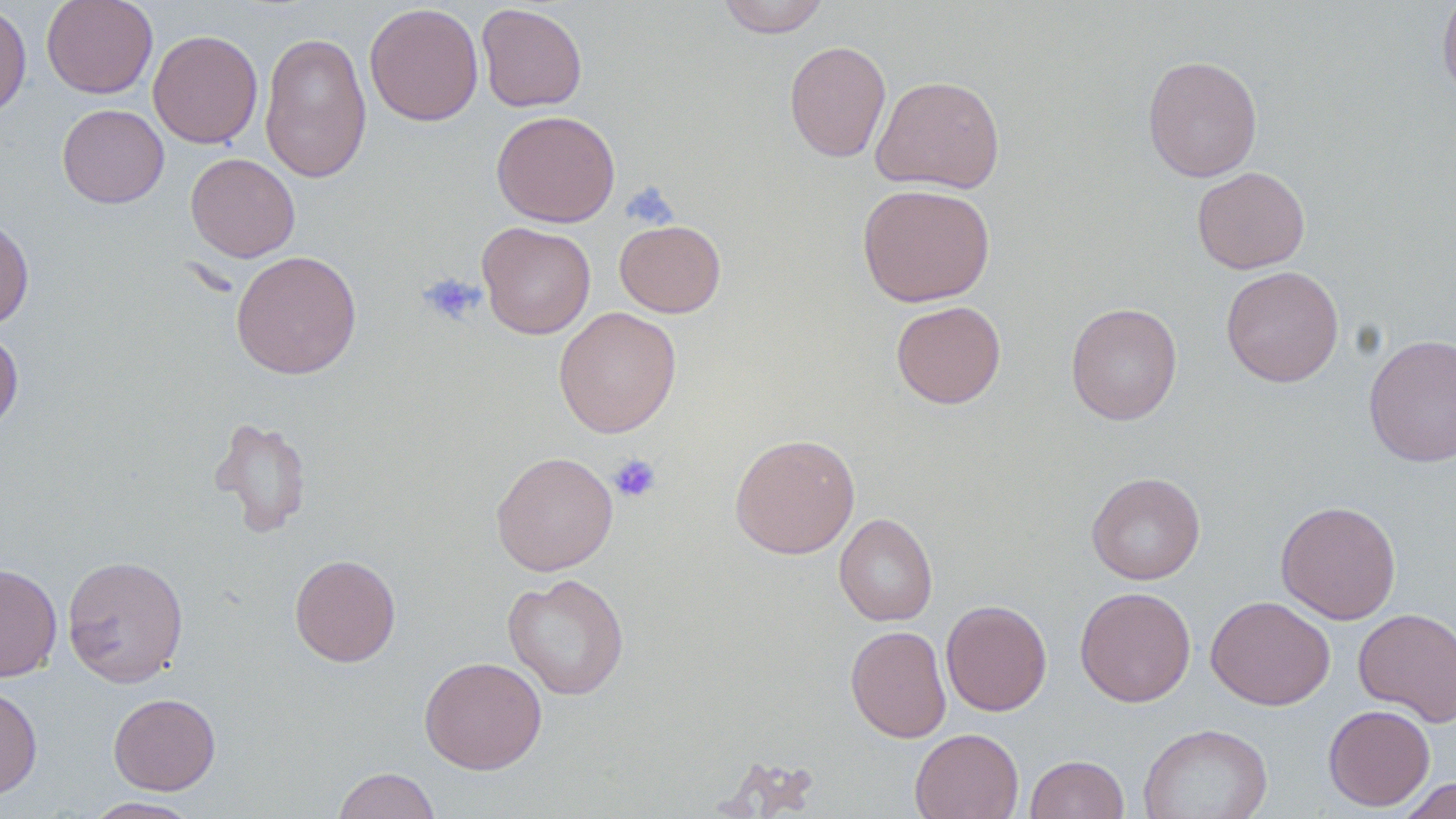
{
  "slide_level_diagnosis": "no evidence of blood parasites",
  "preparation": "thin blood smear",
  "magnification": "1000x",
  "uninfected_red_blood_cell_locations": "approximate bounding boxes as named x1/y1/x2/y2 corners in pixels: (x1=41, y1=0, x2=158, y2=99), (x1=717, y1=0, x2=830, y2=38), (x1=1437, y1=0, x2=1456, y2=106), (x1=0, y1=1, x2=32, y2=122), (x1=364, y1=3, x2=484, y2=126), (x1=476, y1=3, x2=587, y2=112), (x1=148, y1=29, x2=263, y2=149), (x1=259, y1=30, x2=372, y2=183), (x1=784, y1=40, x2=891, y2=163), (x1=1142, y1=55, x2=1263, y2=182), (x1=871, y1=75, x2=1006, y2=193), (x1=57, y1=103, x2=169, y2=208), (x1=491, y1=110, x2=620, y2=227), (x1=186, y1=152, x2=300, y2=262), (x1=1191, y1=166, x2=1310, y2=274), (x1=857, y1=182, x2=996, y2=307), (x1=0, y1=216, x2=34, y2=330), (x1=614, y1=219, x2=726, y2=318), (x1=477, y1=221, x2=596, y2=339), (x1=231, y1=250, x2=362, y2=379), (x1=1221, y1=265, x2=1344, y2=387), (x1=891, y1=300, x2=1006, y2=408), (x1=1066, y1=302, x2=1182, y2=425), (x1=554, y1=306, x2=681, y2=438), (x1=0, y1=328, x2=24, y2=435), (x1=1363, y1=333, x2=1456, y2=468), (x1=209, y1=416, x2=313, y2=538), (x1=729, y1=433, x2=860, y2=559), (x1=491, y1=451, x2=618, y2=576), (x1=1086, y1=471, x2=1205, y2=585), (x1=1275, y1=500, x2=1402, y2=624), (x1=834, y1=512, x2=938, y2=627), (x1=62, y1=554, x2=189, y2=687), (x1=289, y1=554, x2=401, y2=666), (x1=0, y1=563, x2=62, y2=682), (x1=502, y1=573, x2=630, y2=700), (x1=1074, y1=586, x2=1196, y2=707), (x1=1206, y1=595, x2=1336, y2=711), (x1=941, y1=599, x2=1051, y2=716), (x1=1353, y1=608, x2=1455, y2=726), (x1=845, y1=625, x2=951, y2=743), (x1=419, y1=656, x2=547, y2=774), (x1=0, y1=684, x2=42, y2=799), (x1=108, y1=692, x2=221, y2=795), (x1=1323, y1=704, x2=1435, y2=811), (x1=1137, y1=722, x2=1273, y2=819), (x1=909, y1=728, x2=1024, y2=819), (x1=1024, y1=754, x2=1129, y2=819), (x1=332, y1=767, x2=442, y2=819), (x1=1394, y1=777, x2=1456, y2=818), (x1=82, y1=797, x2=204, y2=818)",
  "field_of_view": "single",
  "modality": "light microscopy",
  "platelet_locations": "approximate bounding boxes as named x1/y1/x2/y2 corners in pixels: (x1=623, y1=182, x2=678, y2=229), (x1=418, y1=273, x2=485, y2=327), (x1=609, y1=453, x2=662, y2=504)",
  "stain": "May-Grünwald-Giemsa",
  "image_size": "1456×819 pixels"
}